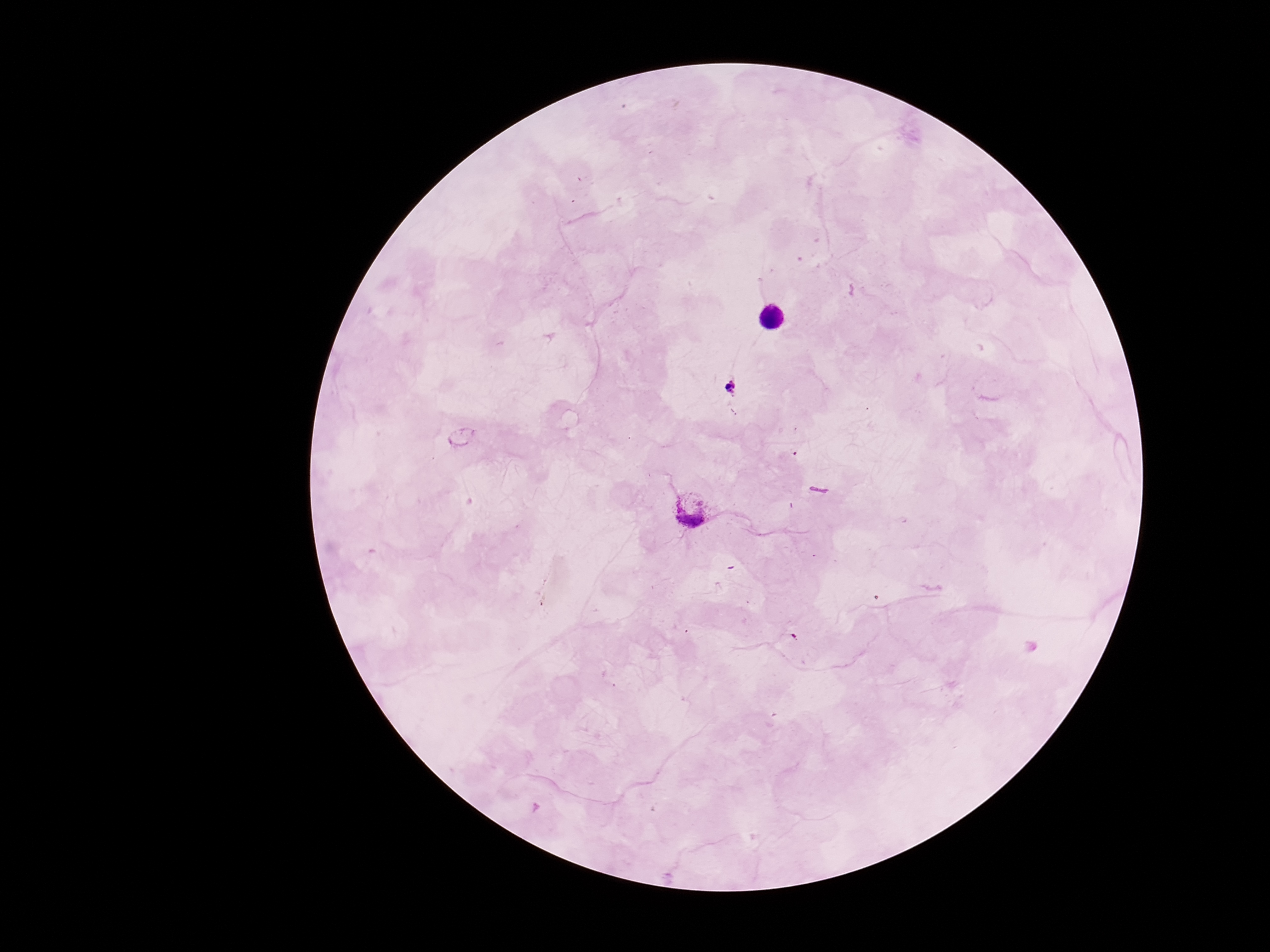
field of view = single
preparation = thick peripheral-blood smear
Plasmodium parasite locations = approximate centers as (x, y) in pixels: (733, 388), (690, 510)
image size = 1270×952 pixels
stain = Giemsa
capture = smartphone camera through the microscope eyepiece
magnification = 100x
patient malaria status = positive